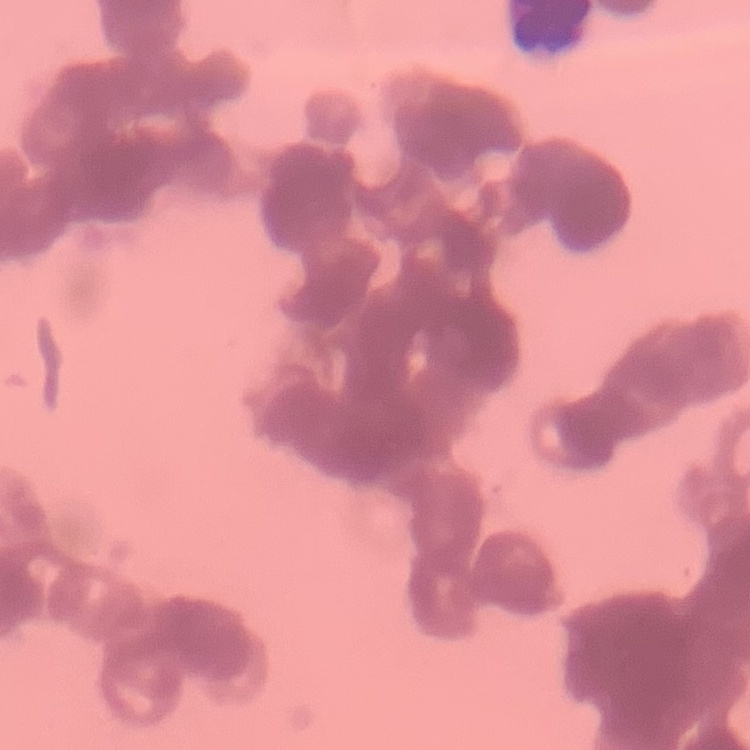

{
  "red_blood_cell_morphology": "rouleaux formation",
  "stain": "Field's or Giemsa",
  "preparation": "thin peripheral smear",
  "image_type": "one tile cut from a larger photomicrograph"
}